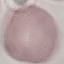
Summary:
  - Malaria status: uninfected
  - Capture: smartphone camera at the microscope eyepiece
  - Preparation: thin blood film
  - Image type: cell patch, automatically extracted from a larger field of view and resized to 64 × 64 pixels
  - Stain: Giemsa